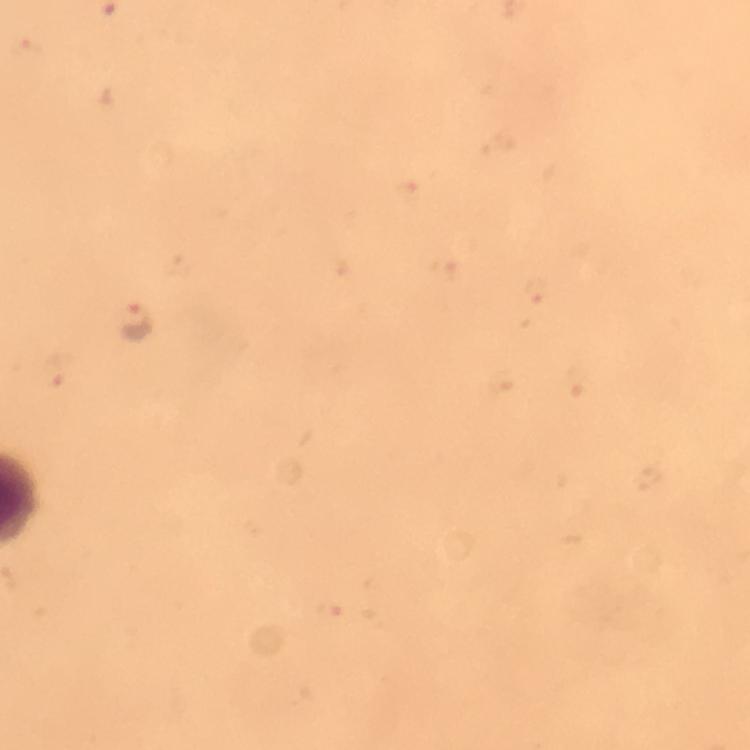

magnification: 100x
context: from a malaria diagnostic workup
capture: smartphone camera through the microscope
image_size: 750×750 pixels
cropped_from: a single field of view
immersion_oil: used
stain: Giemsa
malaria_parasite_locations: 'approximate centers as (x, y) in pixels: (135, 320)'
preparation: thick blood film